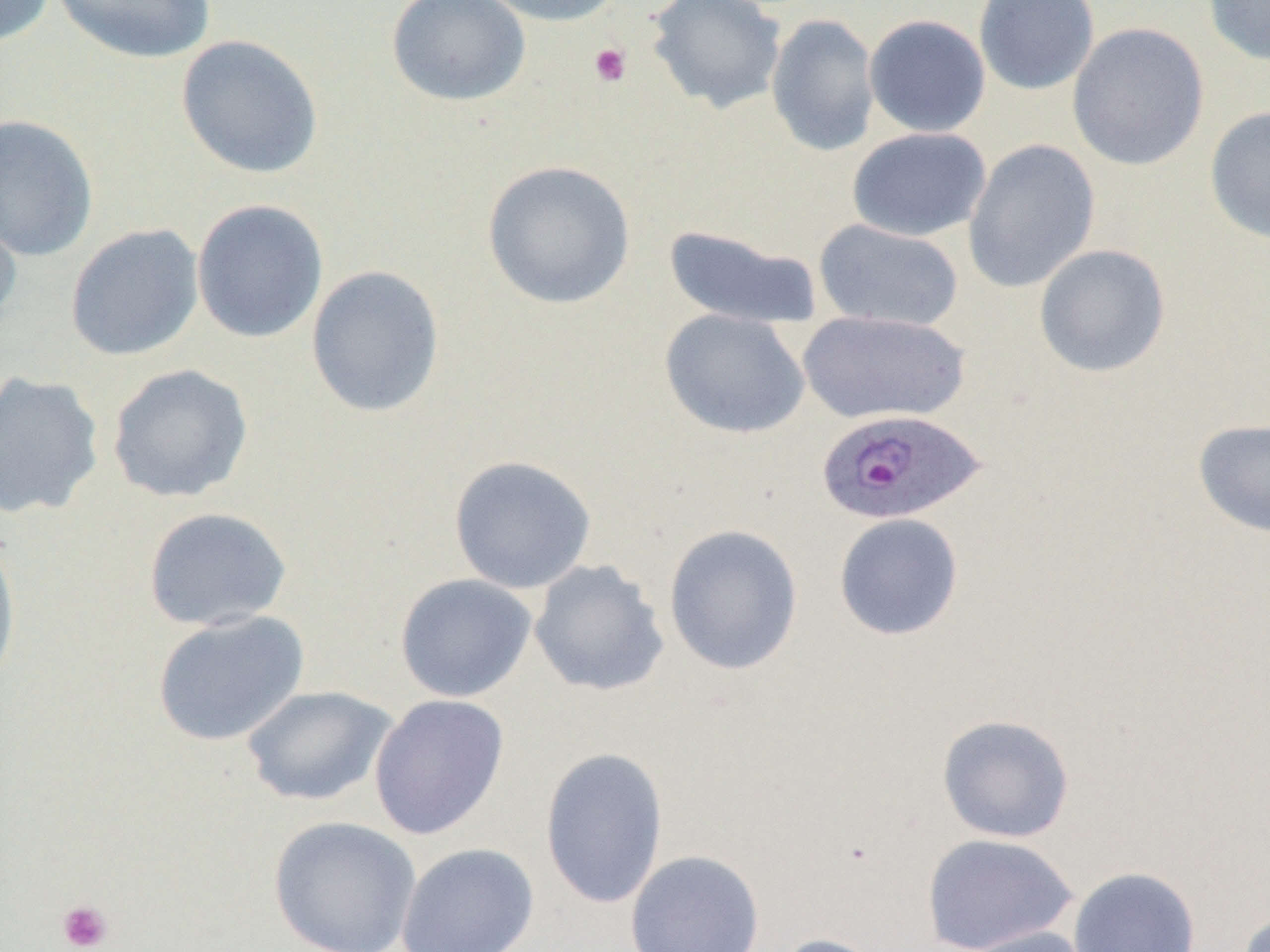

Approximate bounding boxes as named x1/y1/x2/y2 corners in pixels. Platelet locations: (x1=588, y1=43, x2=632, y2=88), (x1=57, y1=899, x2=113, y2=952). Plasmodium ovale-infected red blood cell locations: (x1=815, y1=408, x2=986, y2=526). Uninfected red blood cell locations: (x1=0, y1=0, x2=57, y2=47), (x1=52, y1=0, x2=217, y2=65), (x1=478, y1=0, x2=626, y2=27), (x1=647, y1=0, x2=787, y2=114), (x1=973, y1=0, x2=1100, y2=95), (x1=1203, y1=0, x2=1270, y2=67), (x1=386, y1=1, x2=531, y2=107), (x1=766, y1=13, x2=880, y2=156), (x1=864, y1=14, x2=991, y2=138), (x1=1067, y1=22, x2=1210, y2=172), (x1=176, y1=34, x2=324, y2=179), (x1=1204, y1=106, x2=1270, y2=245), (x1=0, y1=113, x2=99, y2=262), (x1=847, y1=127, x2=991, y2=242), (x1=961, y1=139, x2=1101, y2=292), (x1=482, y1=159, x2=636, y2=309), (x1=0, y1=197, x2=23, y2=334), (x1=191, y1=198, x2=329, y2=344), (x1=813, y1=218, x2=964, y2=332), (x1=64, y1=223, x2=204, y2=361), (x1=662, y1=223, x2=822, y2=330), (x1=1033, y1=243, x2=1171, y2=378), (x1=306, y1=264, x2=445, y2=418), (x1=660, y1=309, x2=809, y2=439), (x1=797, y1=310, x2=970, y2=426), (x1=106, y1=363, x2=254, y2=503), (x1=0, y1=371, x2=105, y2=519), (x1=1192, y1=418, x2=1270, y2=538), (x1=448, y1=455, x2=597, y2=594), (x1=142, y1=506, x2=292, y2=631), (x1=833, y1=512, x2=965, y2=641), (x1=663, y1=523, x2=804, y2=675), (x1=0, y1=534, x2=22, y2=696), (x1=528, y1=559, x2=670, y2=697), (x1=395, y1=573, x2=537, y2=702), (x1=151, y1=610, x2=310, y2=747), (x1=240, y1=684, x2=400, y2=807), (x1=369, y1=693, x2=510, y2=840), (x1=936, y1=713, x2=1075, y2=843), (x1=539, y1=746, x2=671, y2=909), (x1=267, y1=815, x2=422, y2=952), (x1=920, y1=832, x2=1079, y2=952), (x1=396, y1=842, x2=540, y2=952), (x1=625, y1=849, x2=766, y2=952), (x1=1067, y1=867, x2=1201, y2=952), (x1=1235, y1=910, x2=1270, y2=952), (x1=954, y1=925, x2=1096, y2=952), (x1=771, y1=933, x2=887, y2=952). Slide-level diagnosis: Plasmodium ovale. Image is 1270×952 pixels. Thin blood smear. 1000x magnification. Light microscopy. Single field of view.